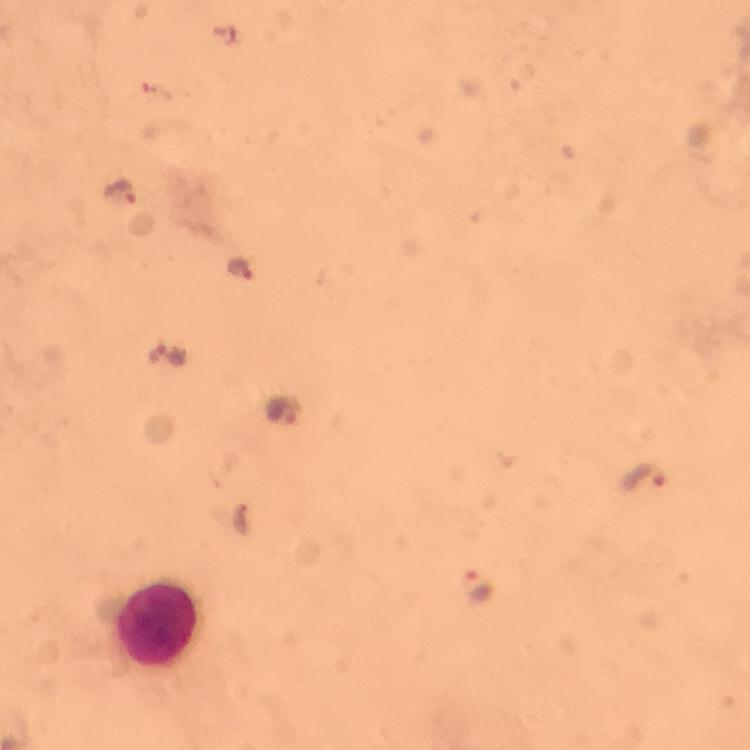

Approximate centers as (x, y) in pixels.
Summary:
  - Leukocyte locations: (155, 621)
  - Plasmodium parasite locations: (120, 195), (243, 269), (287, 408), (646, 481), (477, 586)
  - Capture: smartphone photograph through a microscope
  - Immersion oil: applied
  - Stain: Giemsa
  - Context: from a diagnostic examination for malaria
  - Magnification: 100x
  - Image size: 750×750 pixels
  - Preparation: thick blood smear
  - Cropped from: one field of view